Classify this cell by malaria status.
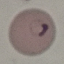
Parasitized.

Acquired by smartphone through the microscope eyepiece. Giemsa stain. Thin smear of blood. Cell patch, automatically extracted from a larger field of view and resized to 64 × 64 pixels.